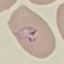
malaria_status: parasitized
image_type: automatically extracted cell patch, resized to 64 × 64 pixels
stain: Giemsa
preparation: thin smear
capture: smartphone camera at the microscope eyepiece